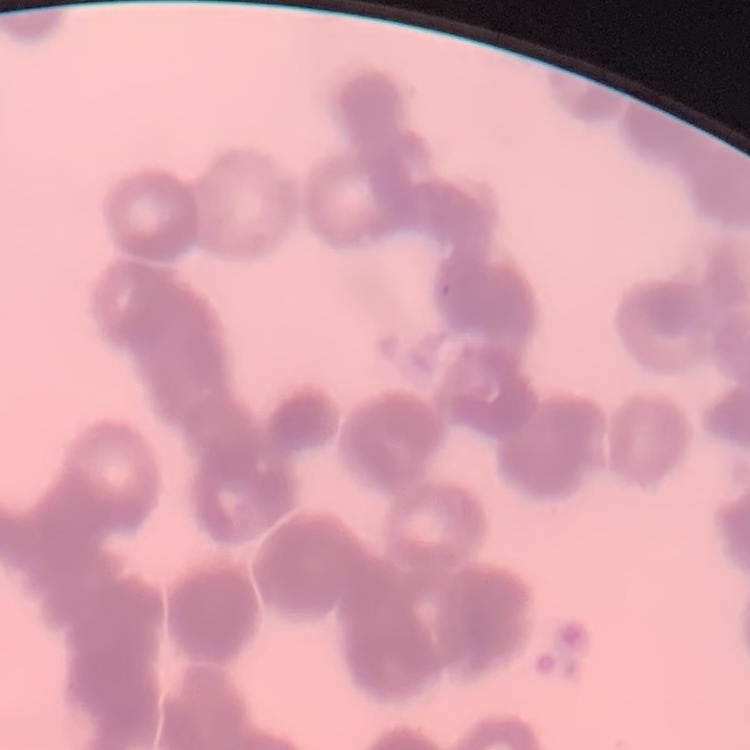
red blood cell morphology = rouleaux formation
stain = Field's or Giemsa
image type = one tile cut from a larger photomicrograph
preparation = thin blood film